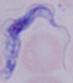
Photomicrograph. A trypanosome is shown. Captured at 1000x magnification.